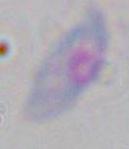

{
  "identification": "Toxoplasma gondii",
  "modality": "micrograph",
  "magnification": "1000x"
}